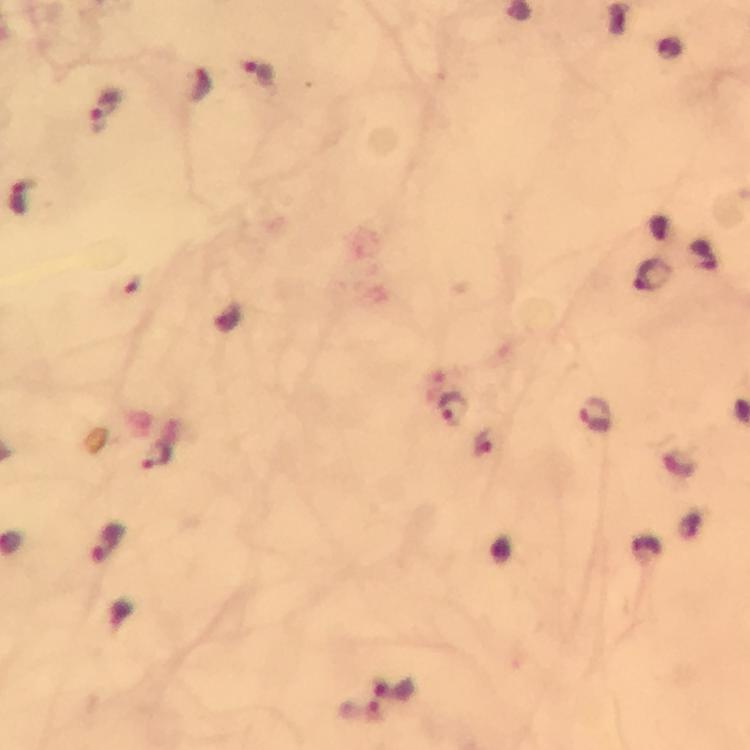
Approximate object centers, in pixels from the top-left corner.
Summary:
  - Malaria parasite locations: (x=257, y=70), (x=107, y=103), (x=22, y=196), (x=651, y=277), (x=455, y=408), (x=597, y=416), (x=158, y=457), (x=106, y=543), (x=395, y=689)
  - Cropped from: one field of view
  - Immersion oil: used
  - Magnification: 100x
  - Preparation: thick smear
  - Capture: smartphone camera through the microscope
  - Context: from a malaria diagnostic workup
  - Stain: Giemsa
  - Image size: 750×750 pixels